Find each parasitized red blood cell.
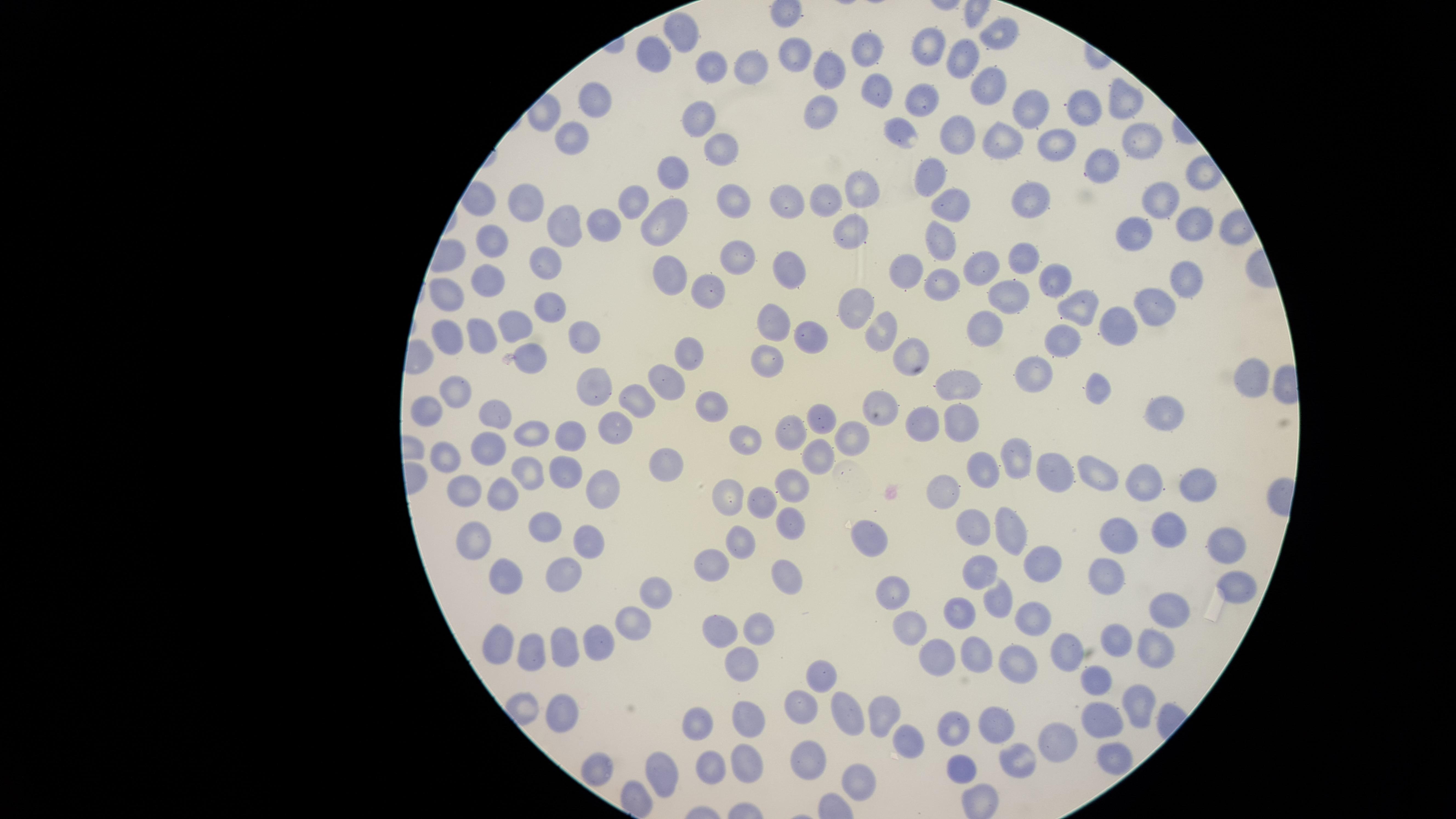
No parasitized red blood cells identified.

Approximate marker points as (x, y) in pixels.
Summary:
  - Uninfected red blood cells: (680, 33), (997, 34), (921, 45), (860, 48), (655, 55), (964, 58), (794, 62), (708, 66), (742, 69), (823, 73), (983, 82), (875, 88), (1130, 92), (596, 95), (920, 95), (1037, 107), (1083, 110), (820, 111), (699, 121), (568, 134), (953, 136), (902, 137), (1137, 140), (1004, 144), (1048, 144), (720, 148), (1105, 165), (928, 176), (664, 177), (861, 185), (633, 195), (1027, 197), (528, 199), (823, 199), (1161, 200), (788, 203), (735, 204), (949, 208), (1197, 218), (664, 222), (607, 225), (564, 226), (845, 230), (494, 237), (937, 240), (1133, 243), (1023, 256), (734, 262), (544, 269), (790, 270), (910, 270), (982, 271), (664, 276), (1175, 281), (1053, 282), (485, 284), (945, 284), (706, 291), (450, 292), (1006, 296), (544, 303), (1153, 303), (1075, 306), (852, 310), (775, 321), (1108, 322), (513, 324), (985, 329), (880, 330), (443, 332), (476, 332), (809, 335), (584, 336), (1064, 339), (527, 351), (688, 352), (769, 354), (909, 357), (1248, 373), (1030, 376), (595, 380), (664, 381), (963, 384), (452, 388), (1096, 391), (709, 400), (632, 405), (878, 406), (1164, 407), (431, 409), (817, 411), (487, 415), (927, 424), (960, 428), (612, 429), (786, 429), (850, 432), (533, 433), (742, 437), (571, 440), (489, 448), (442, 453), (810, 457), (666, 460), (562, 468), (526, 471), (1060, 472), (988, 474), (1107, 475), (608, 480), (1200, 482), (792, 485), (1148, 485), (462, 487), (953, 492), (497, 493), (729, 494), (766, 502), (784, 521), (542, 527), (974, 531), (1014, 532), (1116, 532), (1166, 532), (472, 537), (872, 537), (744, 538), (582, 543), (1218, 545), (1053, 560), (711, 564), (784, 567), (981, 569), (504, 570), (561, 575), (1111, 576), (1236, 588), (648, 590), (889, 593), (994, 600), (1178, 609), (966, 612), (628, 617), (1026, 618), (719, 627), (907, 629), (757, 631), (1114, 636), (497, 639), (595, 639), (563, 645), (1154, 646), (1060, 648), (533, 649), (971, 655), (741, 660), (937, 661), (1012, 662), (821, 679), (1093, 682), (1142, 689), (559, 707), (799, 711), (848, 713), (884, 713), (1101, 717), (749, 719), (695, 725), (989, 727), (948, 728), (904, 741), (1054, 741), (1112, 754), (746, 758), (1022, 761), (811, 764), (598, 765), (966, 765), (705, 769), (662, 775), (861, 781)
  - Image size: 1456×819 pixels
  - Field of view: single
  - Stain: Giemsa
  - Visible region: circular
  - Capture: smartphone photograph through the microscope eyepiece
  - Preparation: thin smear of blood